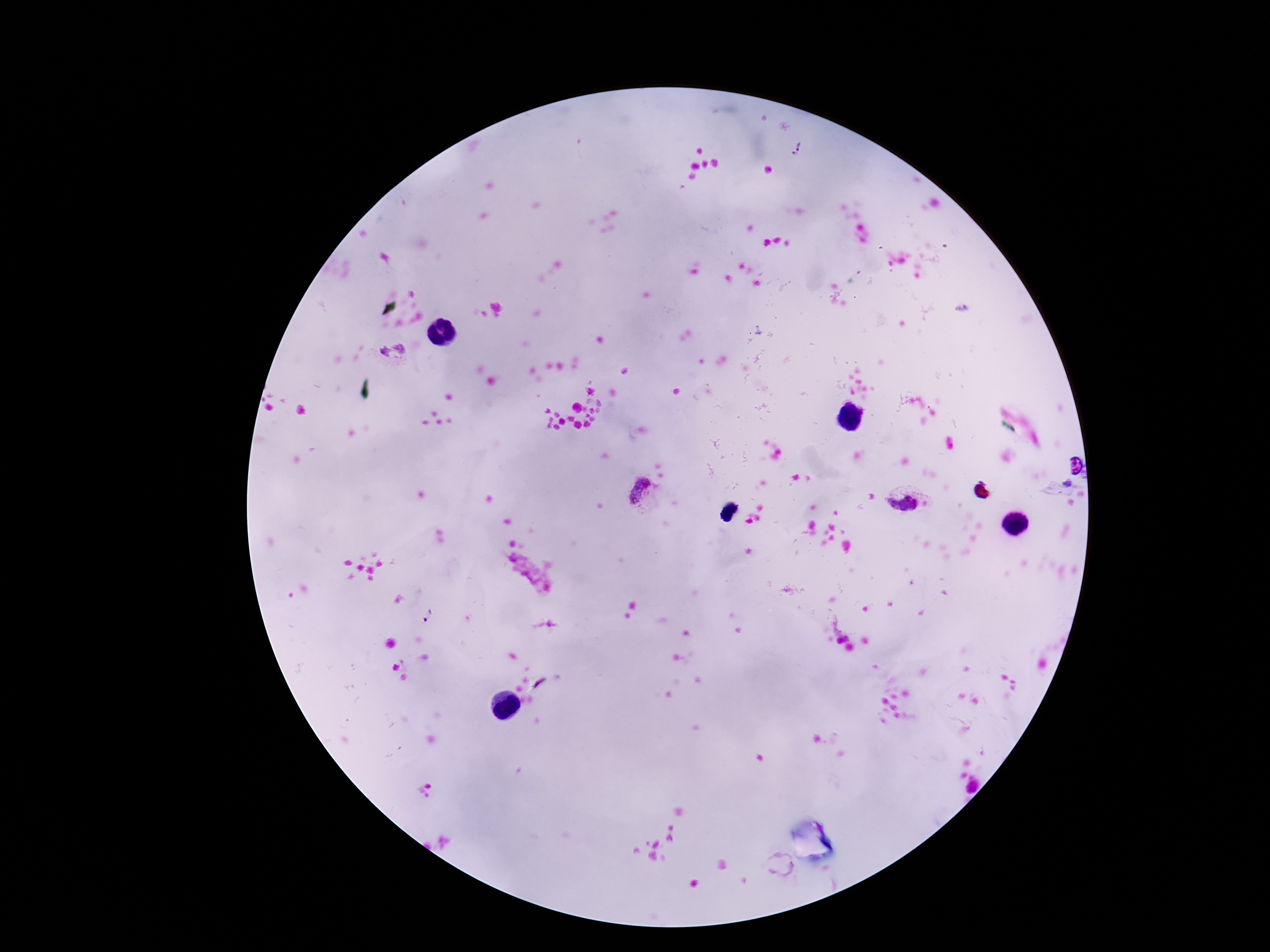

Approximate centers as {x, y} in pixels.
Summary:
  - Plasmodium parasite locations: {798, 149}, {641, 495}, {903, 502}, {529, 572}, {428, 616}, {780, 865}
  - Capture: smartphone camera through the microscope eyepiece
  - Field of view: one from this slide
  - Stain: Giemsa
  - Magnification: 100x
  - Preparation: thick blood smear
  - Patient malaria status: positive
  - Image size: 1270×952 pixels